Report the malaria status of this cell.
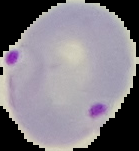

Parasitized.

Summary:
  - Image type: segmented cell region on a black background
  - Image size: 139×151 pixels
  - Preparation: thin blood smear